Give the position of every Plasmodium parasite visible.
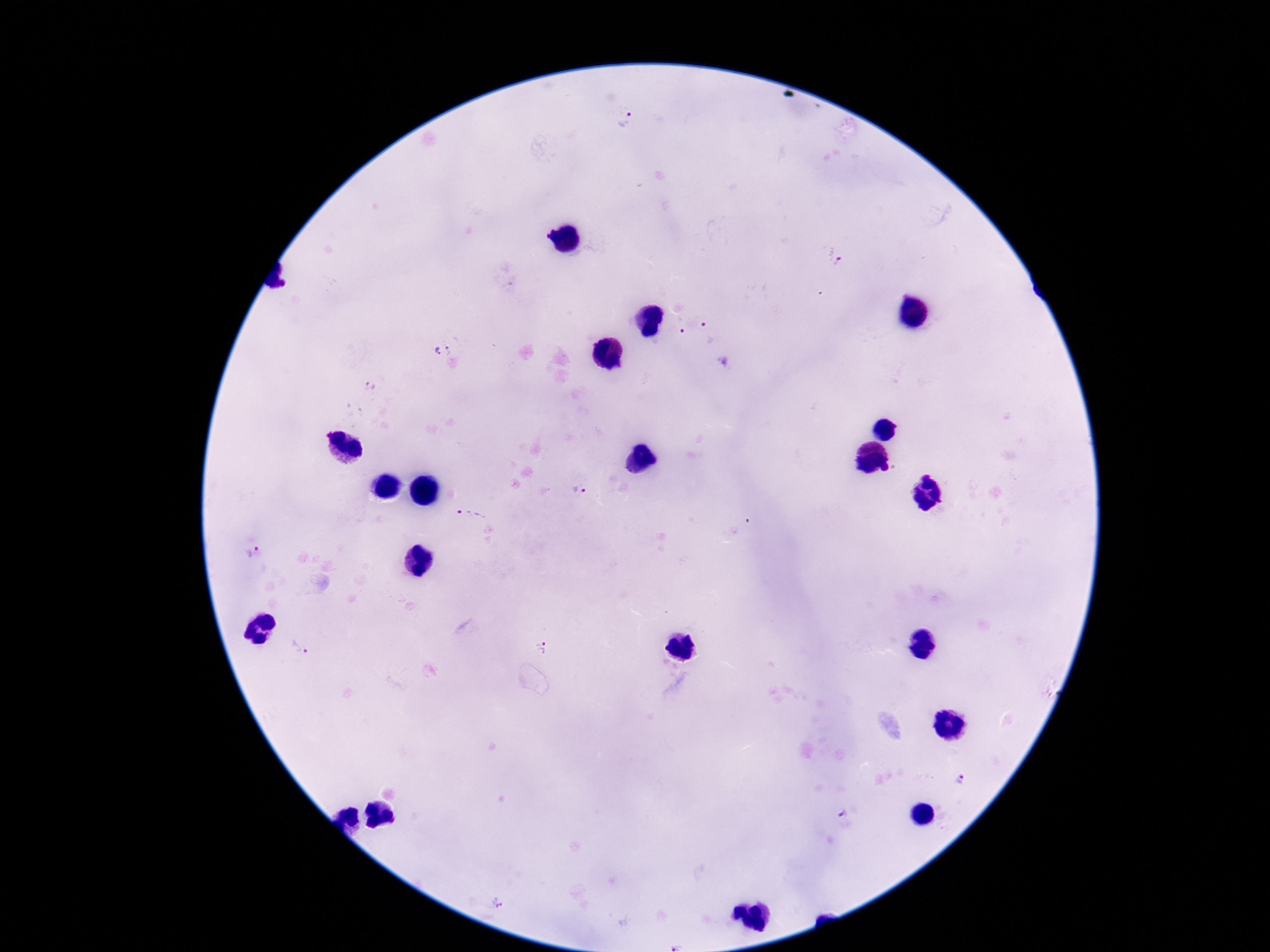

Approximate centers as {x, y} in pixels.
Plasmodium parasites: {626, 119}, {836, 255}, {678, 324}, {704, 325}, {451, 350}, {435, 351}, {371, 386}, {579, 491}, {470, 509}, {254, 553}, {544, 646}, {303, 647}, {961, 781}, {842, 813}, {500, 903}.

{
  "stain": "Giemsa",
  "capture": "smartphone camera through the microscope eyepiece",
  "field_of_view": "single",
  "image_size": "1270×952 pixels",
  "magnification": "100x",
  "preparation": "thick peripheral-blood smear",
  "patient_malaria_status": "positive"
}